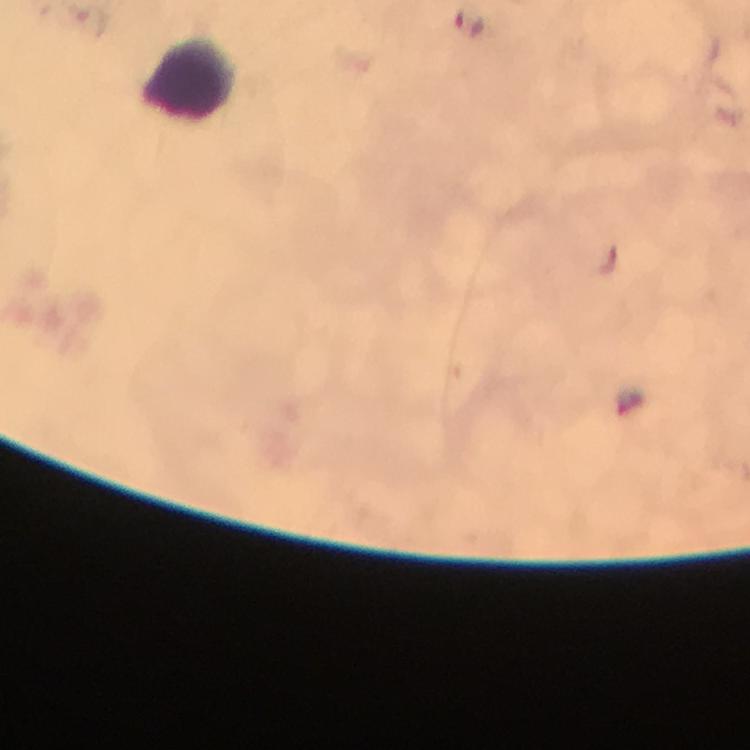
Approximate centers as (x, y) in pixels.
Summary:
  - Leukocyte locations: (190, 80)
  - Image size: 750×750 pixels
  - Preparation: thick blood smear
  - Stain: Giemsa
  - Cropped from: a single field of view
  - Immersion oil: applied
  - Plasmodium parasites: none seen
  - Capture: smartphone camera through the microscope
  - Context: from a diagnostic examination for malaria
  - Magnification: 100x